Describe the morphology of the erythrocytes.
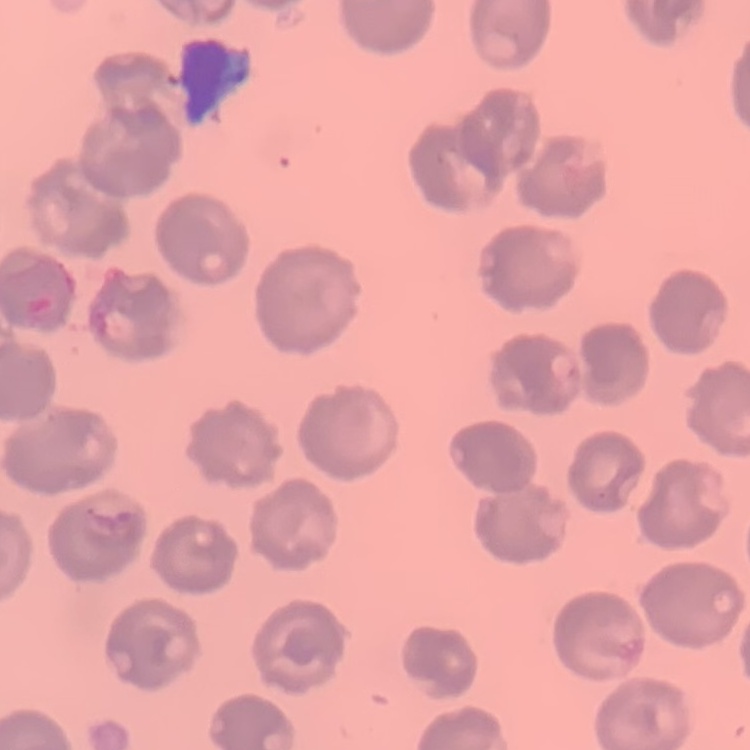
No rouleaux formation.

Summary:
  - Stain: Field's or Giemsa
  - Preparation: thin blood film
  - Image type: one tile cut from a larger photomicrograph